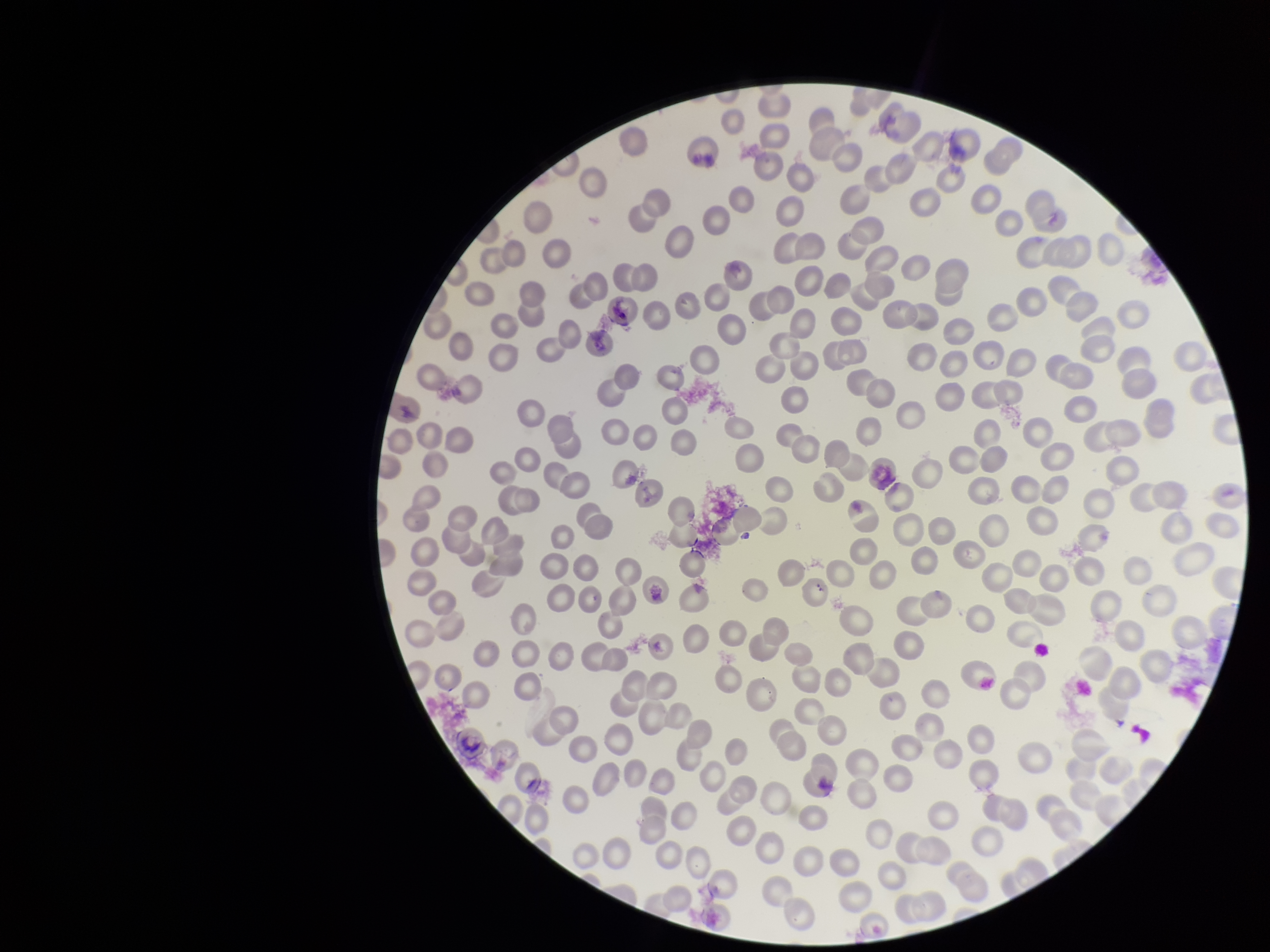

parasitized_red_blood_cells: none identified
field_of_view: single
red_blood_cell_count: 213
parasitized_red_blood_cell_count: 0
preparation: thin blood smear
patient_malaria_status: negative
capture: smartphone photograph through the microscope eyepiece
image_size: 1270×952 pixels
stain: Giemsa